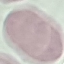
malaria status = uninfected
stain = Giemsa
capture = smartphone camera at the microscope eyepiece
image type = automatically extracted cell patch, resized to 64 × 64 pixels
preparation = thin blood film